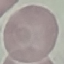

Result: negative for malaria parasites. Thin blood smear. Giemsa stain. Cell patch, automatically extracted from a larger field of view and resized to 64 × 64 pixels. Photographed with a smartphone camera at the microscope eyepiece.